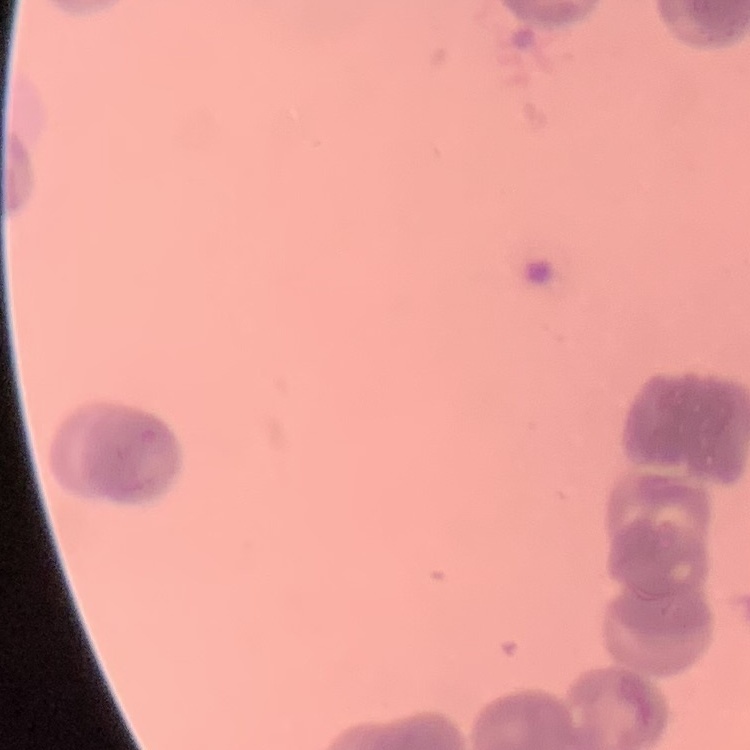

The red blood cells show rouleaux formation. Thin blood film. Field's or Giemsa stain. Square crop of a larger photomicrograph.